Identify the blood parasite species.
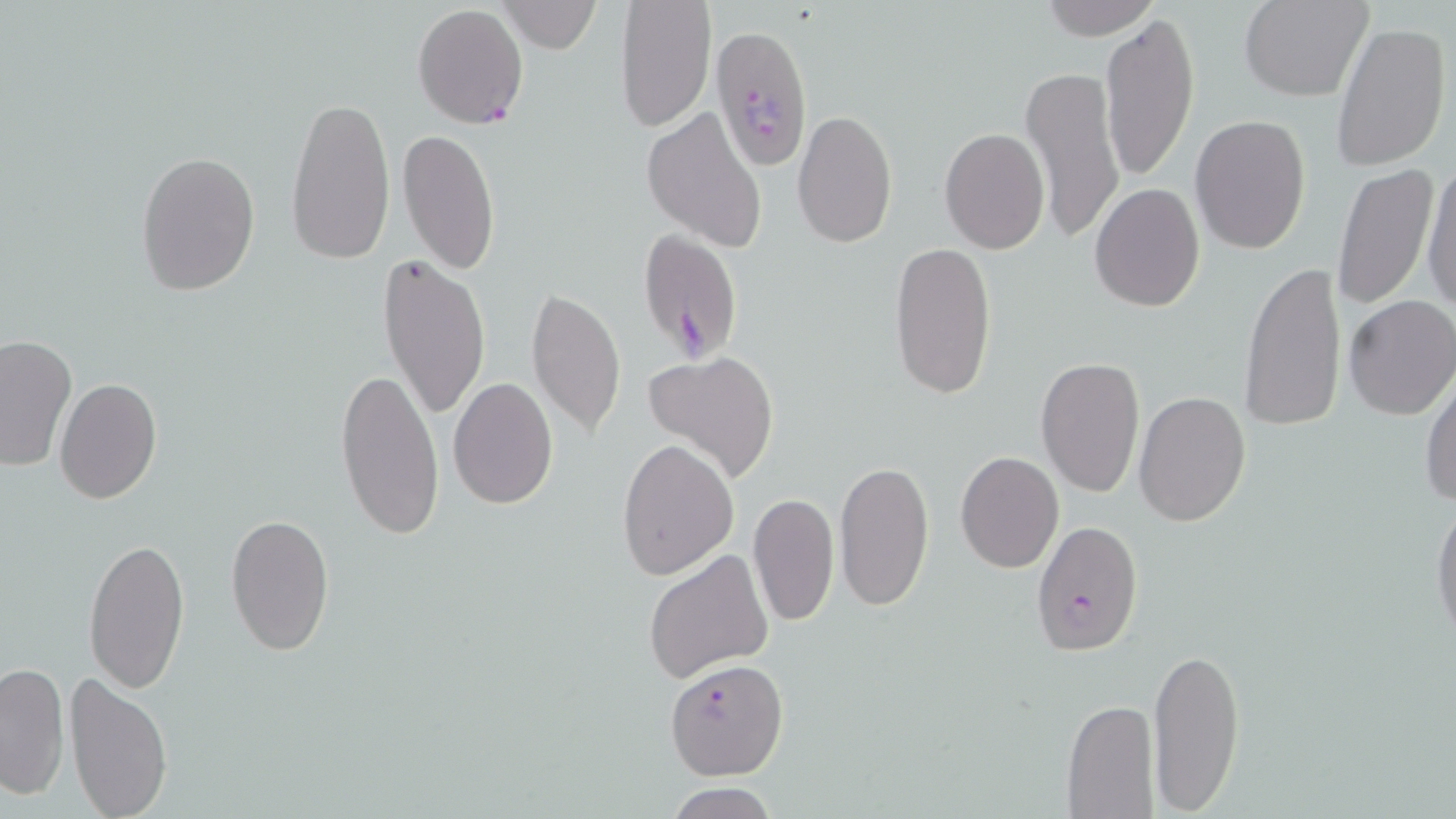
Plasmodium falciparum.

Approximate bounding boxes as [x1, y1, x2, y2] in pixels. Plasmodium falciparum-infected red blood cell locations: [412, 3, 529, 129], [710, 23, 814, 173], [636, 227, 746, 362], [1030, 520, 1142, 658], [664, 657, 788, 780]. Uninfected red blood cell locations: [615, 0, 715, 133], [1238, 0, 1373, 102], [497, 1, 600, 54], [1038, 1, 1163, 40], [1100, 13, 1199, 182], [1330, 18, 1451, 172], [1021, 63, 1125, 245], [285, 95, 396, 263], [641, 106, 767, 254], [792, 108, 898, 249], [1190, 113, 1311, 256], [938, 127, 1050, 255], [397, 128, 501, 274], [135, 150, 261, 297], [1422, 159, 1456, 314], [1331, 161, 1440, 310], [1089, 184, 1205, 313], [887, 241, 999, 401], [377, 251, 490, 428], [1238, 261, 1346, 432], [525, 287, 627, 440], [1343, 295, 1456, 420], [0, 335, 77, 472], [641, 351, 781, 484], [1035, 357, 1147, 498], [336, 364, 443, 544], [1421, 372, 1455, 510], [448, 376, 559, 508], [53, 378, 161, 505], [1133, 391, 1251, 526], [617, 439, 739, 582], [955, 450, 1064, 574], [834, 458, 935, 611], [1429, 490, 1456, 649], [747, 493, 839, 627], [225, 512, 336, 657], [82, 534, 191, 695], [644, 548, 773, 686], [1146, 645, 1247, 812], [0, 661, 70, 799], [64, 671, 173, 818], [1061, 699, 1159, 818], [664, 783, 781, 819]. Light microscopy. Thin blood smear. May-Grünwald-Giemsa-stained preparation. One field of a larger specimen. Image is 1456×819 pixels. 1000x magnification.